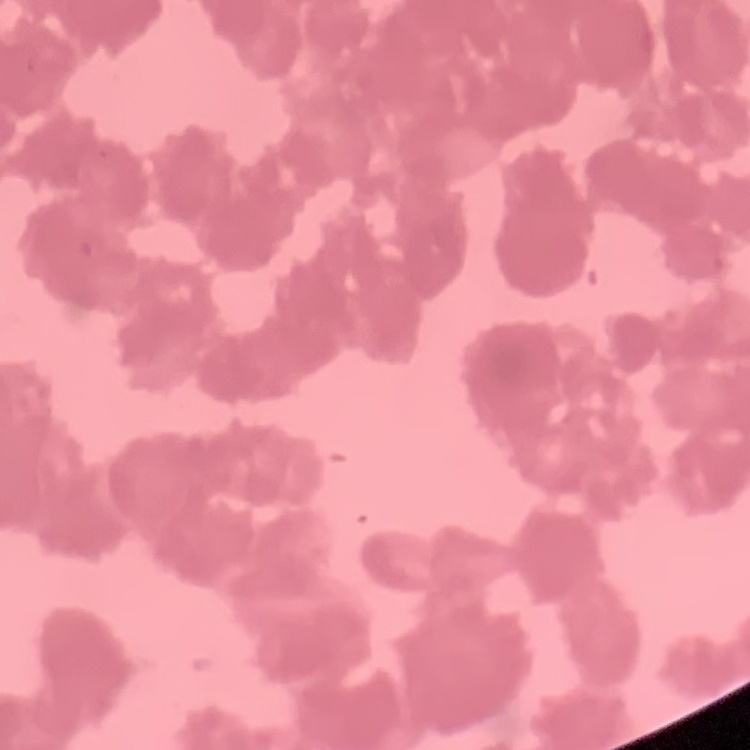

erythrocyte_morphology: rouleaux formation
image_type: one tile cut from a larger photomicrograph
preparation: thin blood smear
stain: Field's or Giemsa